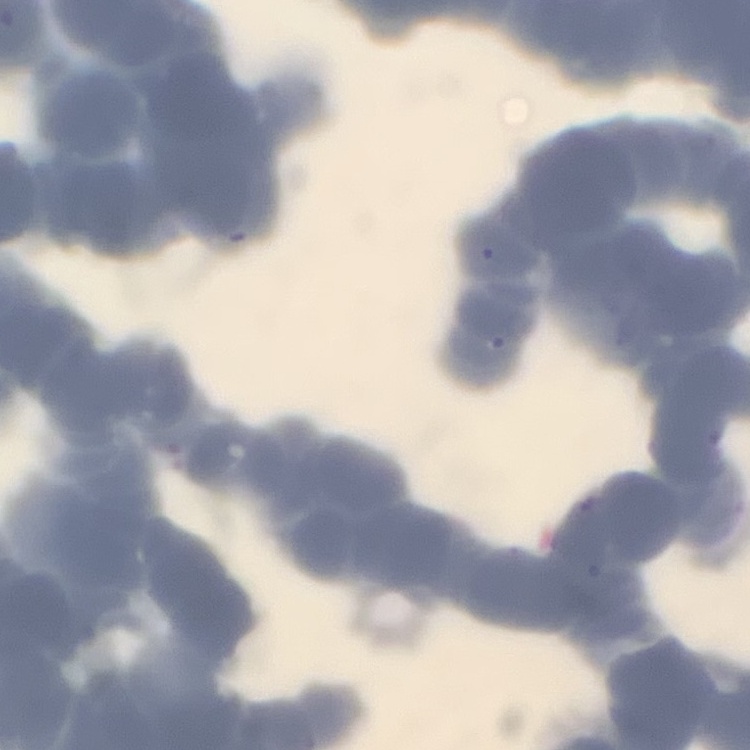
The red blood cells exhibit rouleaux formation. Square crop of a larger photomicrograph. Field's or Giemsa stain. Thin blood smear.